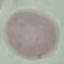
result = negative for malaria parasites
preparation = thin blood smear
stain = Giemsa
capture = smartphone camera at the microscope eyepiece
image type = automatically extracted cell patch, resized to 64 × 64 pixels